Give the position of every leukocyte visible.
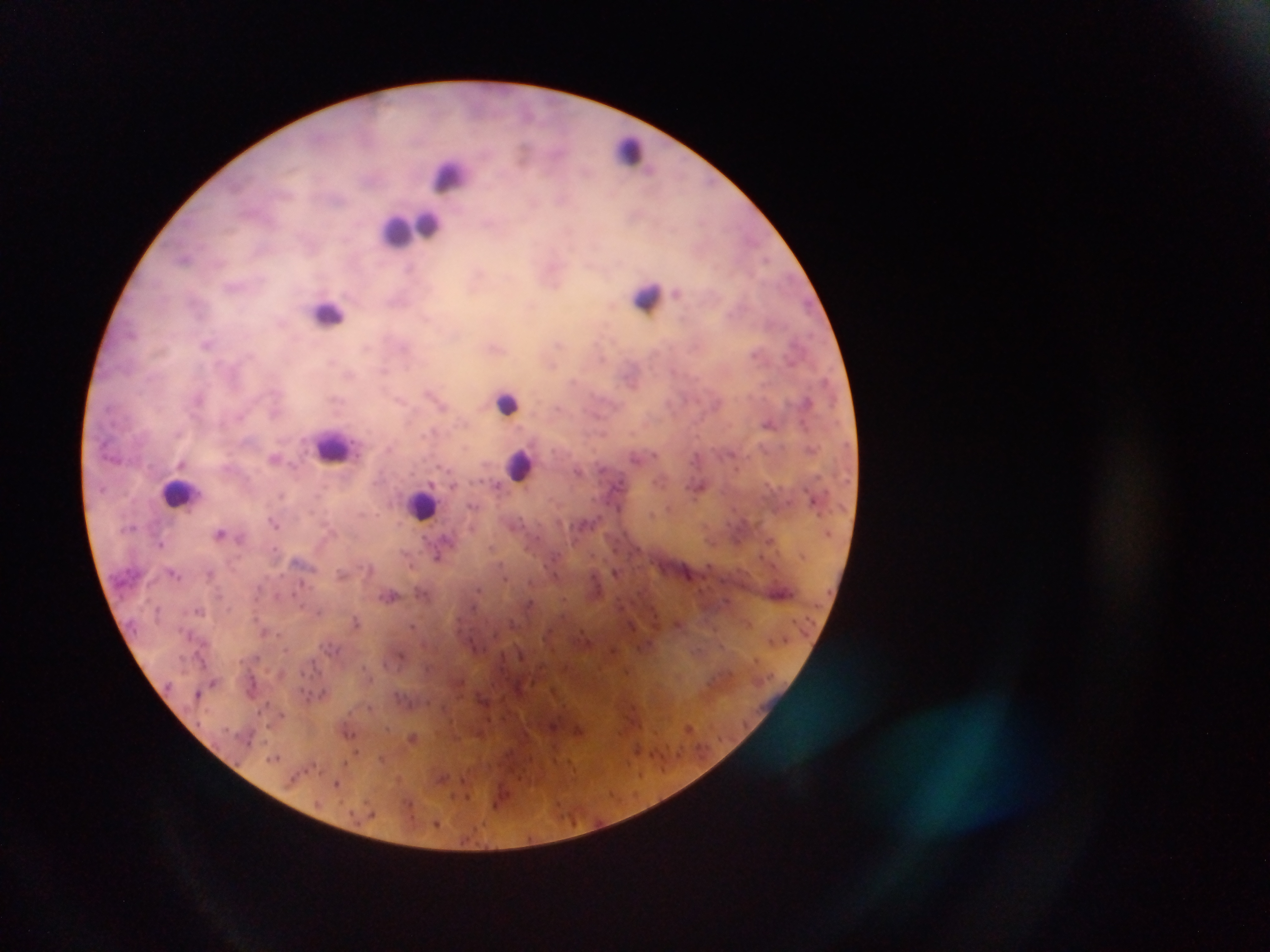
Approximate centers as {x, y} in pixels.
Leukocytes: {630, 150}, {449, 175}, {401, 228}, {647, 297}, {329, 313}, {508, 404}, {333, 447}, {519, 464}, {177, 493}, {423, 503}.

preparation = thick blood smear
capture = mobile-phone photograph through a microscope
malaria parasite locations = approximate centers as {x, y} in pixels: {487, 224}, {184, 258}, {767, 260}, {410, 268}, {676, 292}, {206, 344}, {198, 398}, {808, 401}, {768, 424}, {274, 458}, {181, 463}, {578, 472}, {498, 486}, {617, 486}, {699, 489}, {275, 523}, {220, 533}, {160, 544}, {437, 558}, {616, 572}, {210, 573}, {174, 574}, {341, 574}, {301, 584}, {478, 590}, {391, 596}, {198, 610}, {356, 620}, {412, 626}, {197, 694}, {413, 738}, {274, 758}, {443, 779}, {337, 783}
field of view = single
country = Ghana
image size = 1270×952 pixels